Comment on the morphology of the red blood cells.
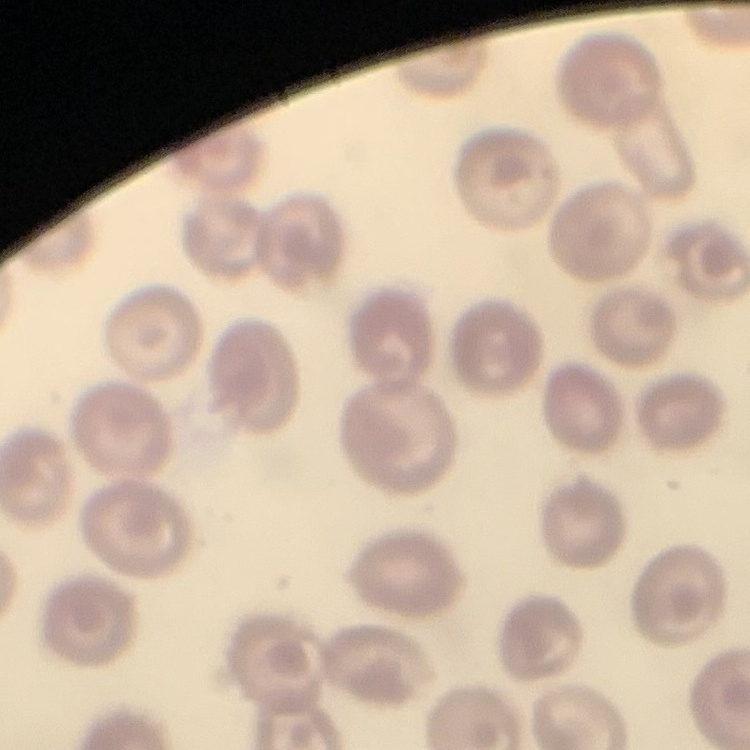
No rouleaux formation.

Summary:
  - Preparation: thin peripheral smear
  - Stain: Field's or Giemsa
  - Image type: one tile cut from a larger photomicrograph